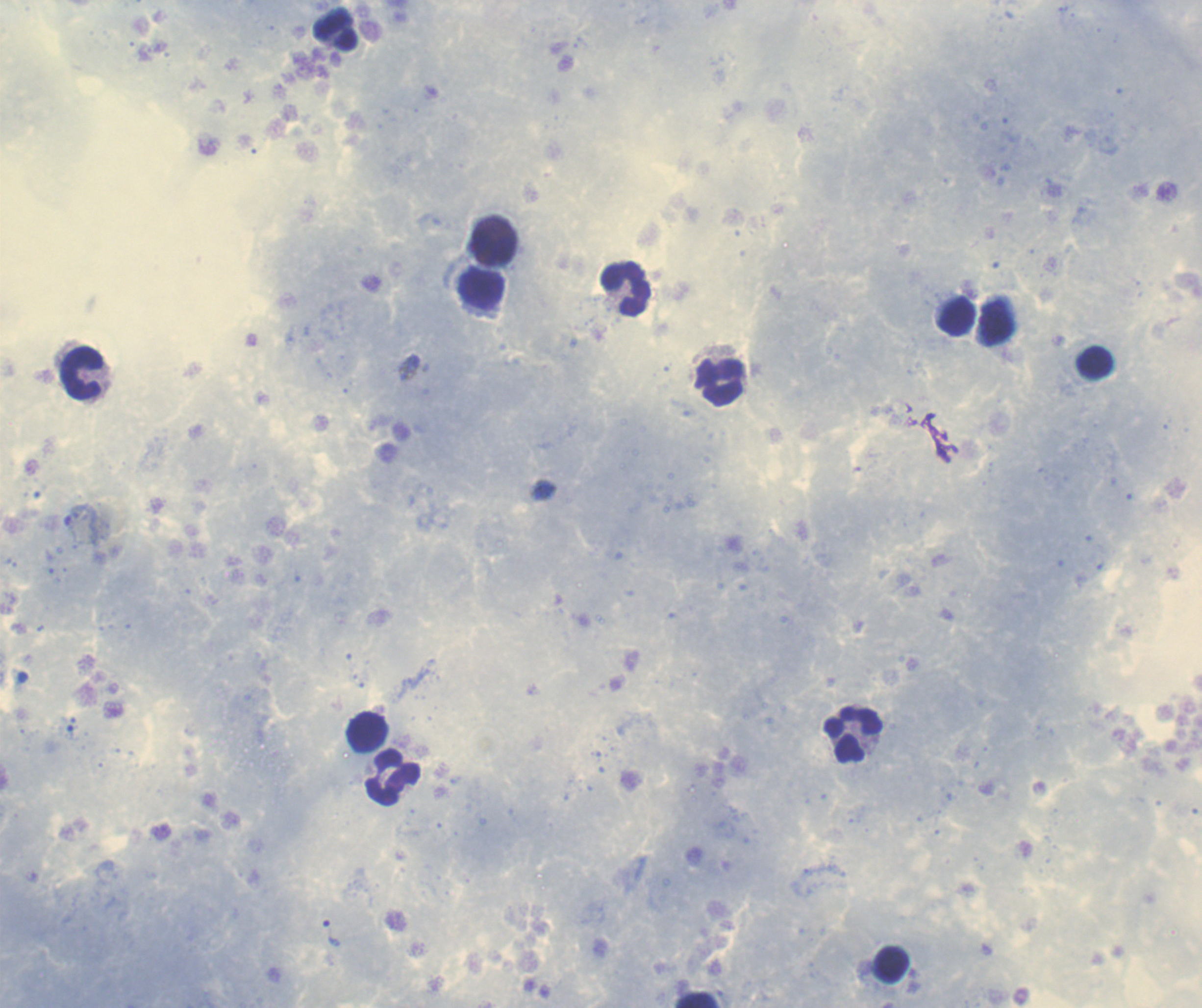 Approximate object centers, in pixels from the top-left corner. Leukocyte locations: (x=335, y=30), (x=494, y=249), (x=481, y=289), (x=625, y=289), (x=956, y=317), (x=1095, y=362), (x=83, y=372), (x=720, y=382), (x=367, y=731), (x=853, y=734), (x=394, y=777), (x=892, y=965), (x=697, y=1001). Trophozoite locations: (x=332, y=933). Image is 1202×1008 pixels. Background quality: good. 100x magnification. Previously used in a real diagnosis. Thick blood smear. Coloration quality: good. Romanowsky stain. Result: Plasmodium parasites identified. One field from this slide.